Outline each uninfected red blood cell.
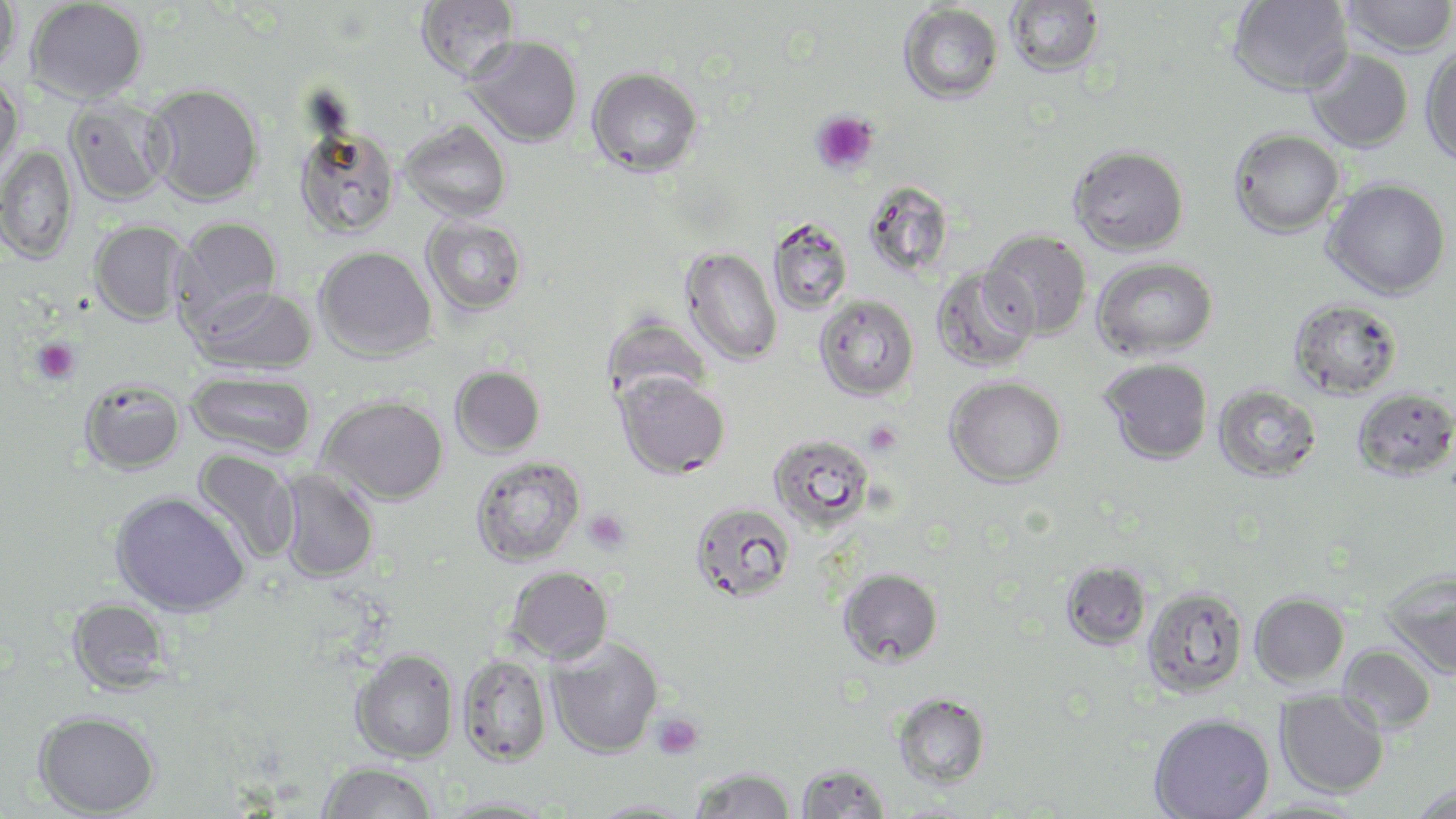

Approximate bounding boxes as named x1/y1/x2/y2 corners in pixels.
Uninfected red blood cells: (x1=0, y1=0, x2=21, y2=78), (x1=26, y1=0, x2=147, y2=104), (x1=416, y1=0, x2=519, y2=81), (x1=1006, y1=0, x2=1104, y2=77), (x1=1228, y1=0, x2=1353, y2=96), (x1=1340, y1=0, x2=1456, y2=57), (x1=898, y1=3, x2=1003, y2=104), (x1=465, y1=36, x2=582, y2=146), (x1=1421, y1=45, x2=1456, y2=167), (x1=1305, y1=49, x2=1413, y2=152), (x1=587, y1=66, x2=703, y2=177), (x1=0, y1=75, x2=24, y2=181), (x1=143, y1=83, x2=264, y2=206), (x1=65, y1=96, x2=172, y2=206), (x1=400, y1=120, x2=512, y2=221), (x1=294, y1=124, x2=401, y2=238), (x1=1229, y1=128, x2=1345, y2=237), (x1=0, y1=144, x2=79, y2=263), (x1=1069, y1=145, x2=1189, y2=255), (x1=1323, y1=179, x2=1453, y2=300), (x1=862, y1=181, x2=954, y2=278), (x1=422, y1=216, x2=528, y2=316), (x1=173, y1=217, x2=283, y2=326), (x1=89, y1=219, x2=188, y2=325), (x1=767, y1=219, x2=853, y2=316), (x1=981, y1=231, x2=1091, y2=340), (x1=314, y1=246, x2=437, y2=361), (x1=681, y1=247, x2=782, y2=366), (x1=1092, y1=257, x2=1218, y2=360), (x1=930, y1=265, x2=1038, y2=373), (x1=191, y1=285, x2=318, y2=374), (x1=814, y1=295, x2=919, y2=401), (x1=1289, y1=298, x2=1403, y2=399), (x1=603, y1=315, x2=712, y2=408), (x1=1101, y1=358, x2=1212, y2=465), (x1=450, y1=365, x2=546, y2=459), (x1=186, y1=370, x2=317, y2=460), (x1=616, y1=371, x2=730, y2=479), (x1=945, y1=376, x2=1066, y2=487), (x1=79, y1=378, x2=185, y2=474), (x1=1214, y1=385, x2=1321, y2=482), (x1=1352, y1=387, x2=1456, y2=481), (x1=318, y1=396, x2=448, y2=505), (x1=768, y1=434, x2=875, y2=531), (x1=192, y1=449, x2=300, y2=564), (x1=470, y1=456, x2=586, y2=567), (x1=275, y1=469, x2=379, y2=583), (x1=110, y1=491, x2=249, y2=618), (x1=690, y1=502, x2=796, y2=604), (x1=1060, y1=561, x2=1152, y2=650), (x1=505, y1=567, x2=614, y2=664), (x1=837, y1=568, x2=944, y2=668), (x1=1381, y1=569, x2=1456, y2=680), (x1=1142, y1=586, x2=1247, y2=698), (x1=1250, y1=592, x2=1349, y2=686), (x1=67, y1=598, x2=172, y2=694), (x1=546, y1=637, x2=663, y2=758), (x1=1339, y1=645, x2=1436, y2=733), (x1=351, y1=649, x2=459, y2=763), (x1=457, y1=654, x2=553, y2=767), (x1=1276, y1=690, x2=1388, y2=797), (x1=893, y1=692, x2=991, y2=790), (x1=33, y1=709, x2=161, y2=817), (x1=1149, y1=713, x2=1275, y2=819), (x1=316, y1=761, x2=437, y2=819), (x1=795, y1=762, x2=891, y2=819), (x1=690, y1=766, x2=795, y2=819), (x1=1408, y1=784, x2=1456, y2=819), (x1=438, y1=796, x2=561, y2=818), (x1=587, y1=798, x2=700, y2=818).

Summary:
  - Platelet locations: (x1=811, y1=110, x2=878, y2=175), (x1=31, y1=338, x2=81, y2=384), (x1=864, y1=421, x2=902, y2=457), (x1=584, y1=509, x2=630, y2=553), (x1=650, y1=712, x2=705, y2=759)
  - Slide-level diagnosis: Plasmodium falciparum
  - Stain: May-Grünwald-Giemsa
  - Magnification: 1000x
  - Modality: light microscopy
  - Preparation: thin blood smear
  - Image size: 1456×819 pixels
  - Field of view: single